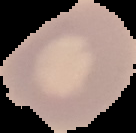
preparation = thin blood film
image type = segmented cell region on a black background
result = no Plasmodium parasites seen
image size = 136×133 pixels